Name the blood parasite species.
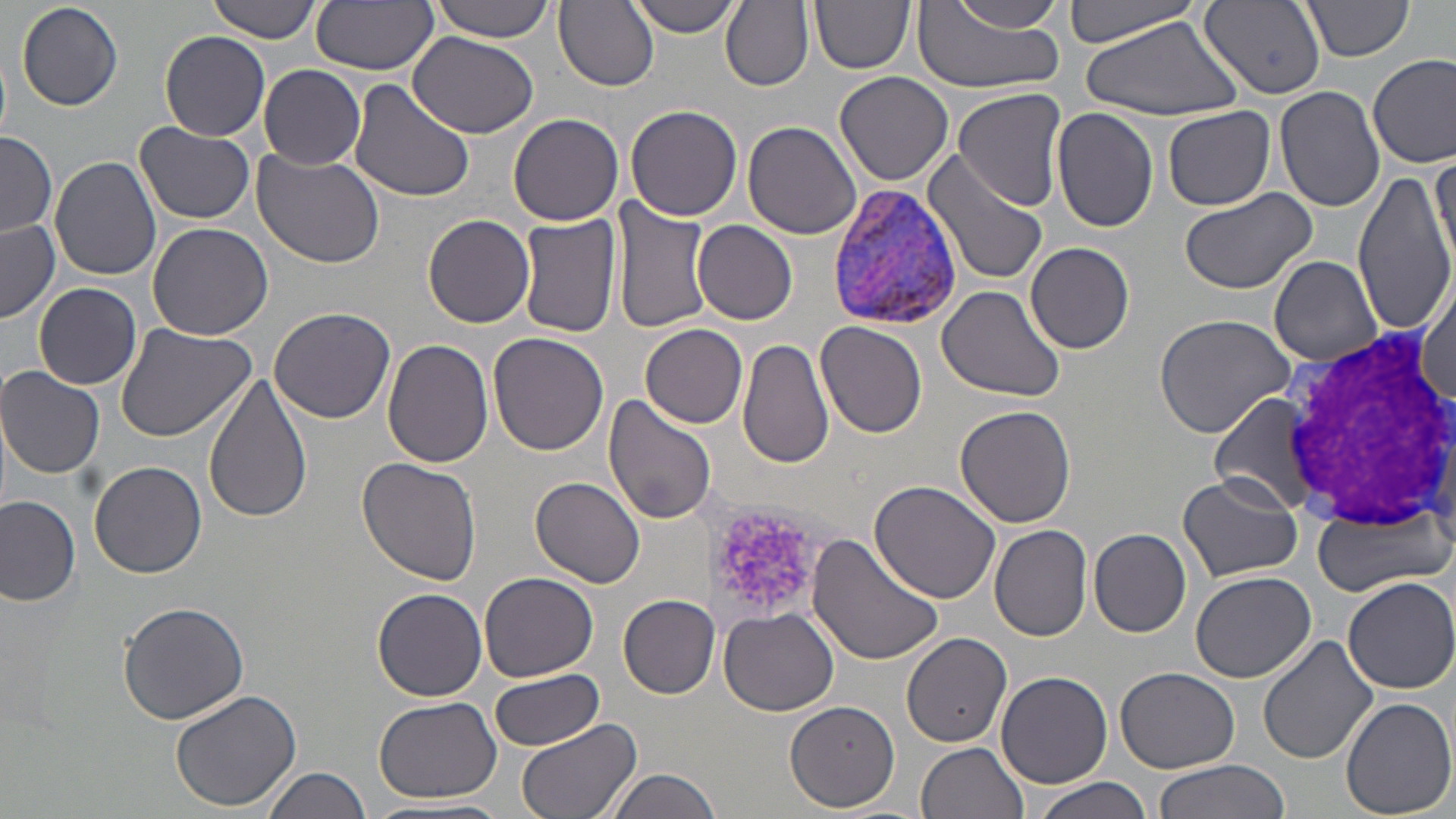
Plasmodium vivax.

Approximate bounding boxes as [x1, y1, x2, y2] in pixels. Plasmodium vivax-infected red blood cell locations: [823, 180, 968, 331]. Uninfected red blood cell locations: [206, 0, 321, 46], [424, 0, 560, 43], [628, 0, 742, 36], [810, 0, 914, 74], [1063, 0, 1208, 49], [311, 1, 438, 75], [555, 1, 658, 90], [721, 1, 813, 91], [933, 1, 1068, 34], [16, 2, 124, 111], [1202, 3, 1326, 99], [1299, 3, 1415, 64], [913, 10, 1065, 95], [1080, 14, 1244, 123], [160, 31, 270, 141], [408, 33, 540, 138], [1, 46, 11, 143], [1369, 53, 1455, 167], [259, 65, 367, 169], [835, 71, 955, 185], [347, 77, 475, 204], [1277, 86, 1387, 213], [954, 87, 1067, 211], [626, 104, 741, 221], [1050, 106, 1159, 232], [1162, 106, 1275, 210], [509, 112, 624, 226], [135, 121, 255, 225], [743, 121, 863, 241], [1, 130, 57, 238], [250, 147, 388, 268], [924, 150, 1052, 289], [1430, 151, 1454, 265], [50, 157, 163, 281], [1353, 169, 1456, 338], [1178, 185, 1315, 296], [608, 196, 713, 335], [516, 212, 622, 339], [423, 215, 536, 328], [692, 219, 798, 325], [0, 220, 59, 324], [146, 220, 275, 340], [1025, 242, 1135, 354], [1269, 256, 1384, 365], [1417, 274, 1455, 414], [33, 283, 142, 389], [937, 285, 1067, 403], [268, 308, 396, 424], [1152, 313, 1298, 439], [816, 321, 928, 439], [116, 322, 257, 444], [641, 324, 749, 429], [488, 334, 609, 456], [739, 337, 835, 470], [384, 339, 495, 468], [0, 365, 105, 478], [203, 372, 314, 525], [604, 395, 718, 525], [1210, 396, 1324, 516], [954, 405, 1077, 529], [357, 458, 483, 586], [89, 460, 207, 577], [1178, 473, 1304, 582], [530, 477, 646, 588], [870, 480, 1003, 606], [0, 497, 82, 604], [1310, 506, 1454, 595], [990, 525, 1093, 641], [1088, 528, 1192, 637], [806, 535, 945, 666], [479, 569, 598, 680], [1191, 571, 1316, 683], [1341, 576, 1456, 694], [373, 587, 487, 701], [618, 593, 721, 697], [117, 603, 249, 724], [719, 608, 839, 716], [901, 631, 1013, 747], [1257, 634, 1381, 767], [1114, 667, 1242, 773], [487, 668, 606, 749], [995, 669, 1112, 787], [171, 688, 301, 812], [373, 694, 503, 804], [1340, 697, 1455, 817], [783, 702, 900, 813], [514, 719, 642, 819], [917, 741, 1030, 819], [1153, 760, 1287, 819], [262, 767, 370, 819], [600, 768, 728, 819], [1026, 775, 1155, 819]. Platelet locations: [705, 503, 834, 628]. White blood cell locations: [1278, 319, 1454, 545]. Thin blood smear. 1000x magnification. One field of a larger specimen. May-Grünwald-Giemsa-stained preparation. Image is 1456×819 pixels. Light microscopy.